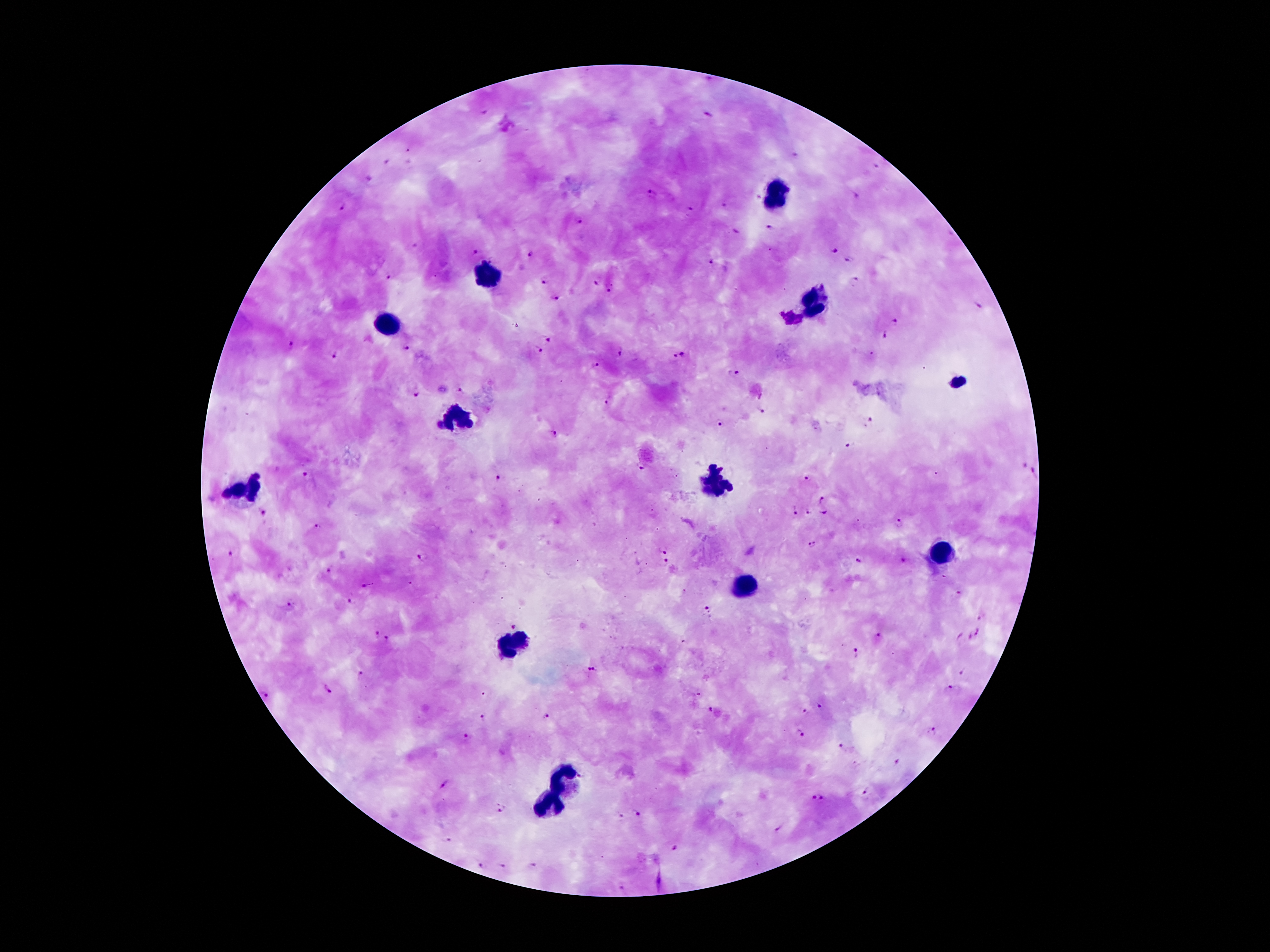

Approximate object centers, in pixels from the top-left corner.
Summary:
  - Leukocyte locations: (x=778, y=195), (x=488, y=275), (x=814, y=303), (x=388, y=325), (x=959, y=381), (x=455, y=417), (x=717, y=483), (x=239, y=491), (x=944, y=554), (x=745, y=587), (x=516, y=641), (x=565, y=779), (x=551, y=804)
  - Plasmodium parasite locations: (x=483, y=112), (x=709, y=116), (x=794, y=156), (x=386, y=163), (x=876, y=168), (x=368, y=178), (x=650, y=193), (x=852, y=195), (x=726, y=205), (x=342, y=206), (x=690, y=210), (x=578, y=219), (x=770, y=229), (x=735, y=232), (x=416, y=244), (x=475, y=250), (x=834, y=251), (x=529, y=253), (x=850, y=258), (x=710, y=264), (x=389, y=276), (x=544, y=281), (x=596, y=282), (x=852, y=282), (x=612, y=289), (x=553, y=298), (x=976, y=304), (x=789, y=319), (x=896, y=321), (x=884, y=335), (x=547, y=338), (x=289, y=345), (x=406, y=345), (x=536, y=349), (x=619, y=351), (x=335, y=353), (x=677, y=357), (x=595, y=366), (x=735, y=373), (x=460, y=388), (x=413, y=393), (x=607, y=402), (x=763, y=412), (x=718, y=422), (x=867, y=423), (x=553, y=434), (x=848, y=444), (x=1024, y=466), (x=638, y=469), (x=1033, y=470), (x=305, y=476), (x=495, y=477), (x=807, y=479), (x=824, y=496), (x=810, y=510), (x=264, y=511), (x=795, y=511), (x=826, y=511), (x=900, y=522), (x=318, y=525), (x=813, y=546), (x=662, y=549), (x=232, y=552), (x=422, y=559), (x=903, y=560), (x=860, y=561), (x=664, y=564), (x=329, y=573), (x=368, y=586), (x=959, y=595), (x=349, y=602), (x=290, y=605), (x=706, y=610), (x=981, y=617), (x=512, y=624), (x=980, y=631), (x=377, y=634), (x=881, y=637), (x=959, y=637), (x=970, y=637), (x=387, y=639), (x=854, y=655), (x=595, y=668), (x=964, y=670), (x=363, y=672), (x=327, y=687), (x=951, y=688), (x=265, y=692), (x=699, y=692), (x=820, y=704), (x=711, y=708), (x=804, y=709), (x=548, y=715), (x=484, y=716), (x=932, y=730), (x=801, y=732), (x=465, y=736), (x=842, y=747), (x=897, y=762), (x=444, y=783), (x=865, y=793), (x=817, y=797), (x=499, y=805), (x=637, y=812), (x=619, y=816), (x=445, y=840), (x=677, y=847), (x=502, y=864), (x=479, y=865), (x=532, y=865), (x=621, y=887)
  - Stain: Giemsa
  - Capture: smartphone through the microscope eyepiece
  - Image size: 1270×952 pixels
  - Magnification: 100x
  - Preparation: thick peripheral-blood smear
  - Field of view: one from this slide
  - Patient malaria status: positive for Plasmodium falciparum